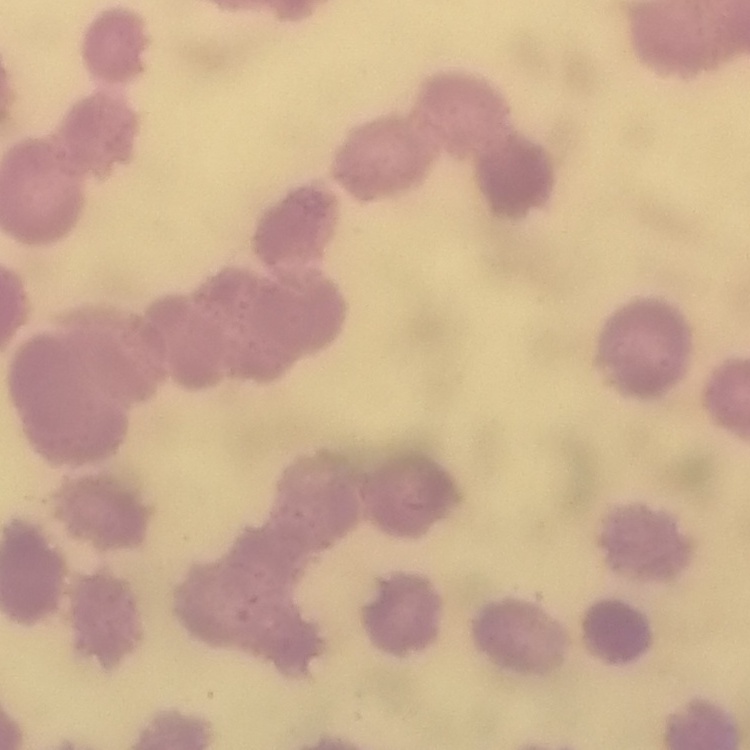
The erythrocytes show rouleaux formation. One tile cut from a larger photomicrograph. Field's or Giemsa stain. Thin peripheral smear.